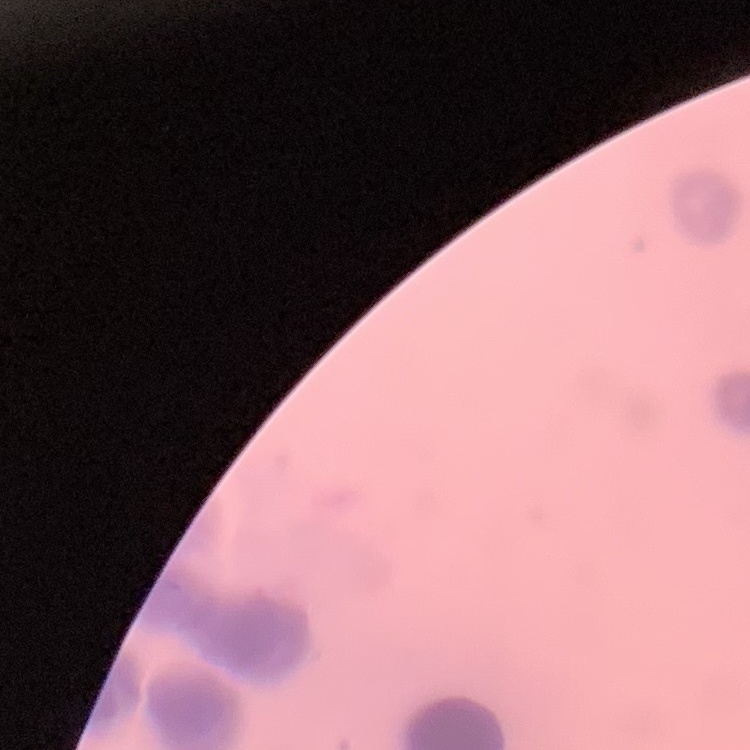
red blood cell morphology = rouleaux formation
preparation = thin blood film
stain = Field's or Giemsa
image type = square crop of a larger photomicrograph